State the blood parasite species.
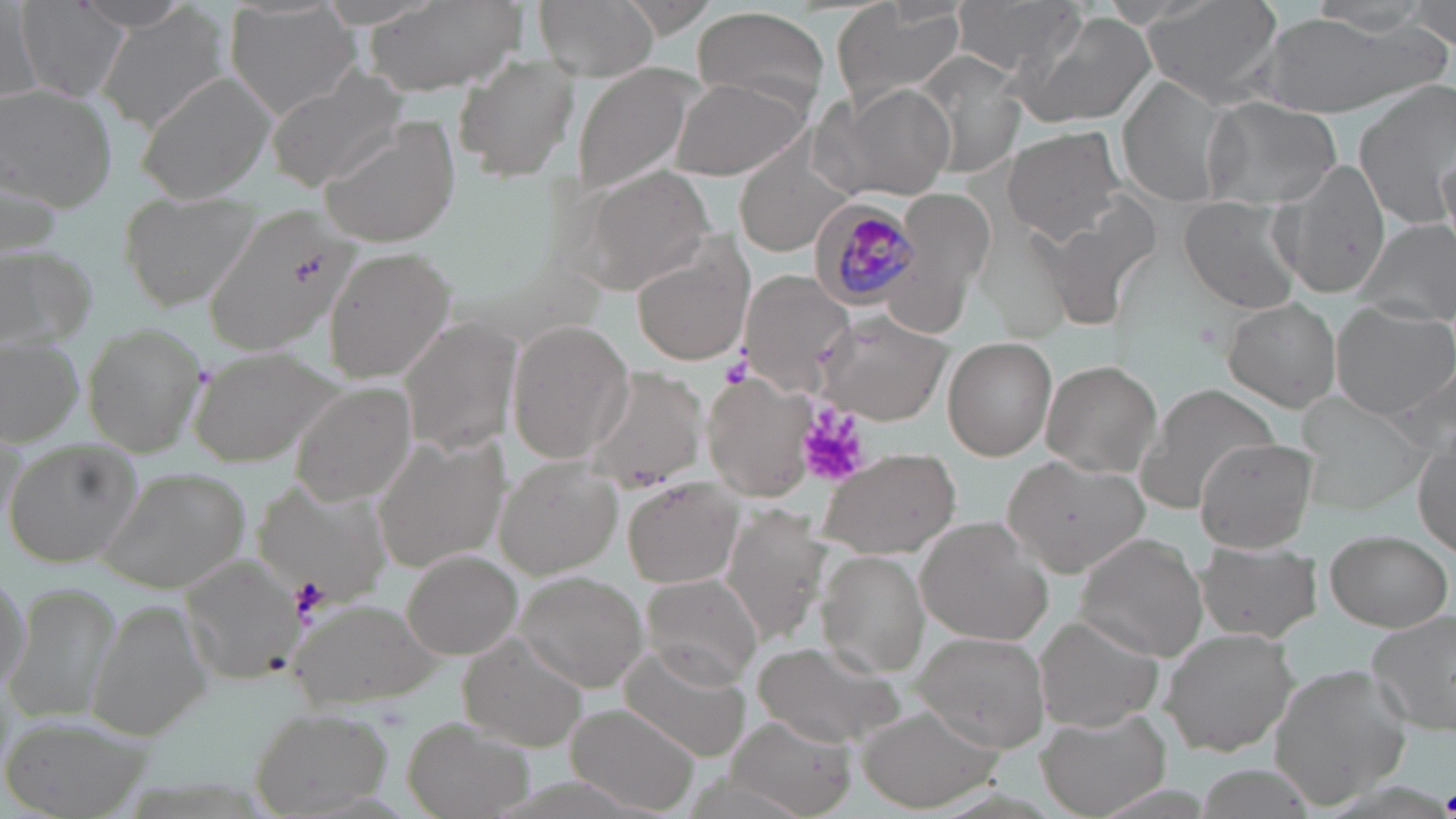
Plasmodium malariae.

Approximate bounding boxes as [x1, y1, x2, y2] in pixels. Plasmodium malariae-infected red blood cell locations: [811, 200, 920, 307]. Uninfected red blood cell locations: [71, 0, 198, 33], [223, 0, 361, 119], [363, 0, 524, 98], [531, 0, 660, 80], [829, 0, 969, 115], [952, 0, 1091, 81], [1139, 0, 1287, 105], [15, 1, 130, 107], [1302, 1, 1443, 40], [3, 2, 43, 108], [96, 3, 231, 132], [690, 6, 833, 113], [1405, 7, 1455, 50], [1016, 9, 1157, 131], [1254, 10, 1434, 120], [832, 16, 994, 194], [907, 52, 1028, 181], [453, 55, 583, 184], [571, 66, 699, 197], [266, 69, 407, 191], [134, 70, 277, 203], [669, 76, 809, 181], [1120, 77, 1233, 206], [816, 79, 958, 203], [1353, 81, 1456, 227], [1, 84, 115, 210], [1202, 96, 1340, 209], [319, 116, 463, 246], [1003, 124, 1127, 242], [736, 145, 854, 257], [1434, 151, 1455, 249], [1275, 157, 1390, 297], [572, 164, 718, 294], [884, 185, 995, 324], [121, 192, 264, 311], [1179, 197, 1302, 314], [207, 208, 363, 359], [1355, 219, 1455, 327], [630, 235, 755, 367], [0, 244, 94, 348], [325, 248, 454, 381], [738, 270, 859, 392], [1224, 298, 1341, 412], [1332, 301, 1454, 419], [814, 308, 954, 424], [399, 318, 522, 455], [506, 320, 634, 463], [81, 324, 206, 456], [940, 335, 1056, 459], [1, 338, 83, 443], [185, 344, 350, 468], [1043, 362, 1160, 476], [583, 364, 711, 492], [701, 379, 814, 499], [291, 382, 420, 507], [1137, 382, 1279, 509], [1296, 394, 1429, 512], [370, 433, 509, 578], [1194, 437, 1318, 551], [5, 439, 142, 571], [1414, 443, 1455, 554], [815, 447, 960, 561], [1004, 454, 1150, 575], [496, 455, 624, 577], [101, 466, 246, 593], [623, 478, 741, 589], [253, 480, 393, 607], [724, 502, 826, 642], [915, 518, 1054, 645], [1324, 530, 1451, 633], [1074, 532, 1210, 661], [1194, 544, 1320, 643], [403, 551, 523, 659], [819, 552, 931, 676], [180, 555, 303, 684], [0, 563, 32, 704], [513, 572, 648, 692], [640, 574, 764, 689], [5, 582, 123, 725], [84, 601, 212, 740], [292, 601, 452, 711], [1367, 611, 1456, 738], [1036, 613, 1166, 733], [1161, 626, 1302, 756], [459, 633, 588, 751], [913, 633, 1052, 752], [753, 639, 906, 748], [620, 645, 752, 762], [1268, 662, 1412, 807], [568, 704, 701, 815], [858, 706, 1002, 811], [248, 707, 391, 815], [1038, 710, 1169, 816], [0, 712, 159, 818], [729, 715, 853, 819], [402, 717, 531, 817]. Platelet locations: [722, 351, 752, 386], [798, 412, 867, 487], [289, 576, 328, 617], [1443, 787, 1456, 815]. Image is 1456×819 pixels. Light microscopy. Captured at 1000x magnification. One field of a larger specimen. May-Grünwald-Giemsa stain. Thin blood film.